Locate every blood parasite and identify its species.
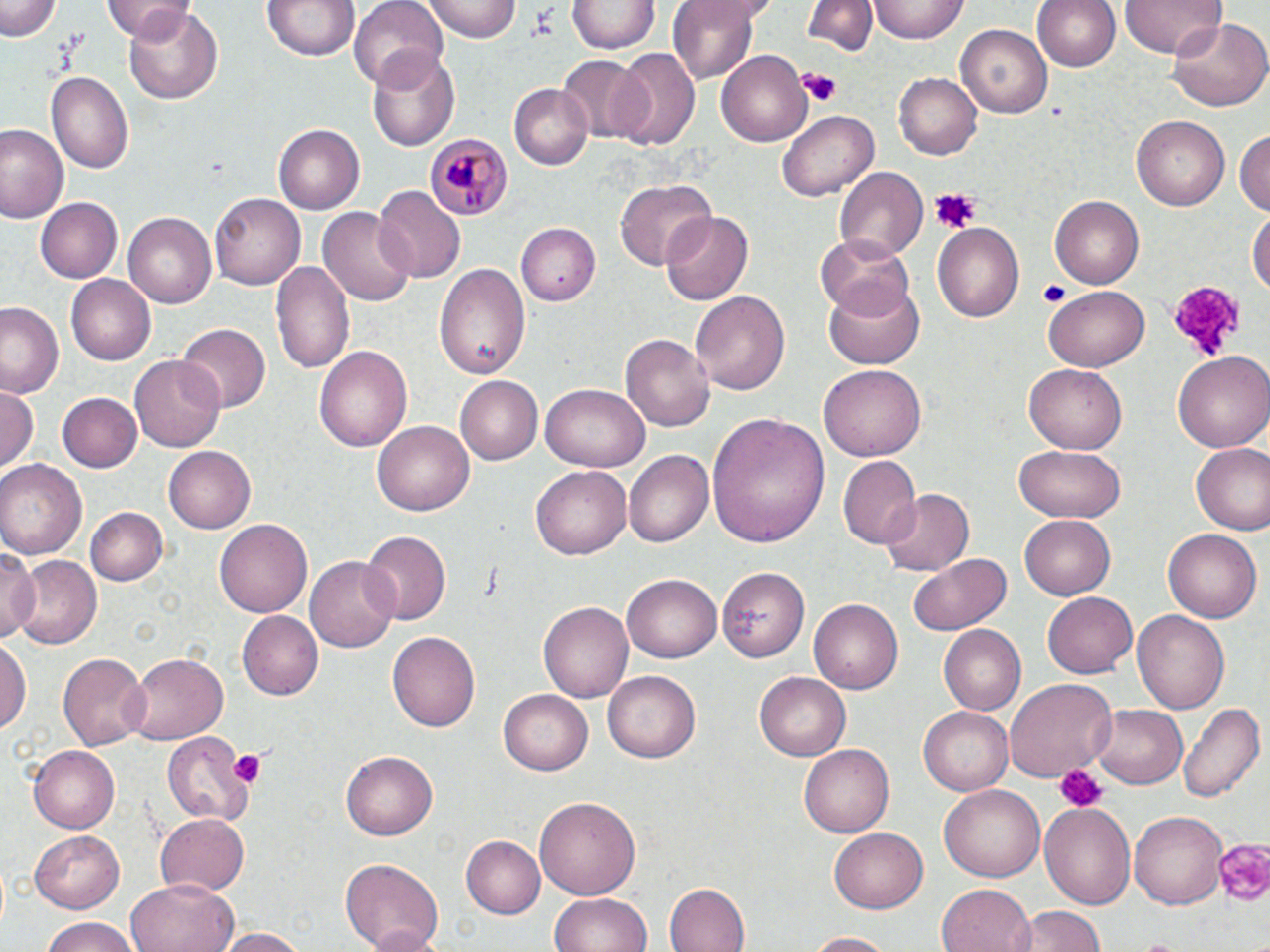

Approximate bounding boxes as (x1, y1, x2, y2) in pixels.
Plasmodium malariae-infected red blood cells: (428, 132, 513, 222).
No Plasmodium falciparum, Plasmodium ovale, Plasmodium vivax, Babesia divergens, or Trypanosoma brucei observed.

{
  "slide_level_diagnosis": "Plasmodium malariae",
  "field_of_view": "single",
  "stain": "May-Grünwald-Giemsa",
  "platelet_locations": "approximate bounding boxes as (x1, y1, x2, y2) in pixels: (796, 68, 841, 106), (928, 187, 979, 232), (1038, 280, 1068, 305), (1167, 280, 1249, 360), (227, 747, 268, 789), (1053, 762, 1109, 813), (1212, 834, 1268, 905)",
  "image_size": "1270×952 pixels",
  "preparation": "thin blood film",
  "uninfected_red_blood_cell_locations": "approximate bounding boxes as (x1, y1, x2, y2) in pixels: (2, 0, 63, 42), (102, 0, 195, 41), (263, 0, 360, 61), (347, 0, 449, 88), (424, 0, 519, 40), (669, 0, 759, 84), (868, 0, 969, 42), (1030, 0, 1122, 73), (1120, 0, 1223, 59), (569, 1, 657, 54), (806, 1, 876, 56), (125, 4, 223, 102), (1167, 19, 1268, 112), (956, 24, 1053, 119), (612, 48, 702, 151), (367, 50, 461, 150), (717, 52, 810, 145), (557, 56, 652, 143), (45, 72, 134, 176), (895, 72, 981, 161), (510, 84, 593, 169), (778, 109, 878, 201), (1132, 115, 1230, 210), (273, 123, 364, 214), (0, 124, 68, 226), (1233, 129, 1270, 218), (834, 165, 927, 263), (613, 178, 718, 271), (373, 188, 466, 282), (209, 194, 305, 291), (1050, 195, 1145, 288), (36, 198, 122, 282), (318, 208, 414, 306), (1248, 208, 1270, 300), (660, 209, 753, 305), (122, 212, 216, 308), (933, 223, 1026, 323), (520, 224, 601, 304), (818, 235, 916, 317), (269, 261, 354, 376), (434, 264, 530, 381), (67, 275, 156, 365), (823, 277, 926, 370), (1043, 285, 1149, 371), (690, 290, 790, 397), (0, 300, 65, 399), (177, 323, 272, 412), (620, 332, 717, 431), (314, 344, 412, 452), (1173, 350, 1270, 452), (129, 355, 227, 451), (820, 365, 928, 462), (1022, 365, 1128, 454), (454, 376, 543, 466), (541, 381, 649, 469), (0, 385, 38, 471), (59, 393, 142, 473), (708, 411, 829, 546), (372, 421, 472, 516), (1190, 443, 1270, 535), (1015, 445, 1124, 521), (164, 447, 255, 532), (625, 451, 712, 547), (837, 456, 921, 550), (0, 459, 87, 555), (530, 465, 631, 561), (879, 487, 974, 578), (83, 507, 168, 586), (1020, 515, 1116, 599), (214, 519, 310, 617), (1163, 528, 1261, 624), (360, 531, 449, 625), (0, 548, 40, 642), (907, 550, 1008, 635), (11, 555, 101, 648), (305, 555, 402, 654), (718, 566, 808, 661), (622, 571, 722, 660), (1042, 591, 1138, 679), (808, 598, 906, 695), (538, 600, 633, 701), (1132, 609, 1231, 716), (235, 611, 322, 700), (937, 625, 1027, 715), (388, 630, 481, 732), (1, 636, 29, 742), (58, 651, 151, 748), (125, 653, 229, 743), (604, 671, 702, 763), (754, 672, 849, 760), (1007, 678, 1117, 782), (498, 690, 594, 777), (1177, 699, 1264, 806), (1090, 701, 1188, 788), (920, 706, 1011, 796), (164, 730, 262, 820), (800, 743, 894, 837), (27, 745, 119, 831), (342, 750, 438, 841), (939, 784, 1045, 882), (535, 796, 641, 901), (1040, 801, 1137, 913), (153, 811, 250, 895), (1131, 813, 1226, 909), (829, 826, 927, 913), (28, 829, 126, 912), (462, 835, 545, 917), (339, 856, 443, 952), (126, 878, 237, 952), (663, 883, 749, 952), (936, 884, 1035, 952), (548, 894, 654, 952), (1021, 905, 1107, 951), (38, 918, 144, 952), (215, 927, 311, 952), (801, 930, 901, 950)",
  "modality": "light microscopy",
  "magnification": "1000x"
}